State the preparation type.
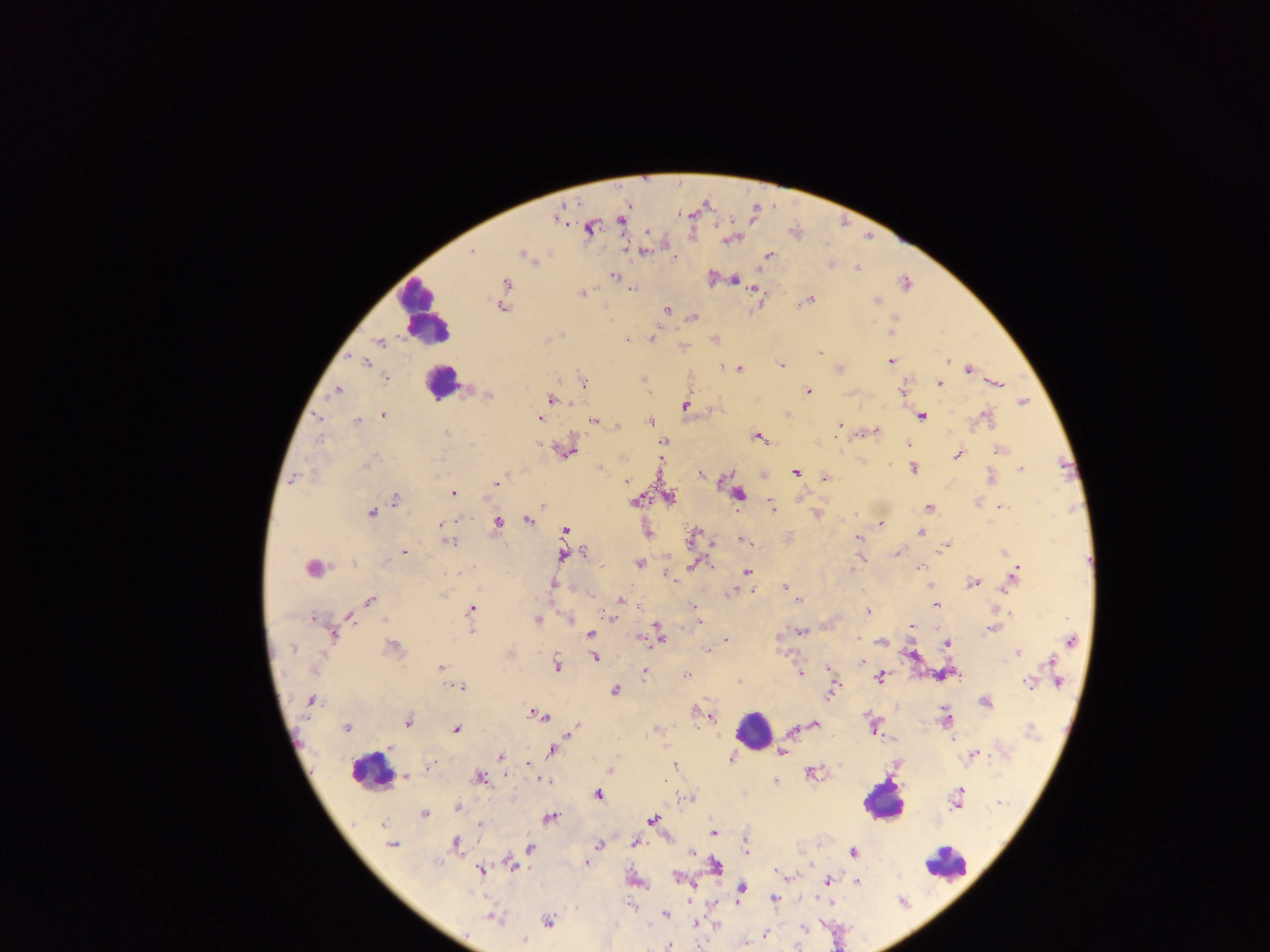

This is a thick smear.

Approximate centers as {x, y} in pixels. Leukocyte locations: {424, 313}, {441, 382}, {753, 730}, {374, 765}, {882, 801}, {948, 865}. Malaria parasite locations: {589, 228}, {646, 232}, {729, 240}, {472, 252}, {643, 252}, {522, 254}, {769, 255}, {830, 264}, {857, 267}, {614, 276}, {734, 280}, {906, 283}, {506, 284}, {633, 288}, {755, 289}, {581, 293}, {810, 300}, {876, 301}, {503, 307}, {668, 309}, {693, 317}, {893, 328}, {652, 338}, {627, 340}, {379, 342}, {820, 351}, {363, 361}, {948, 361}, {890, 362}, {781, 365}, {722, 366}, {740, 369}, {969, 369}, {839, 370}, {387, 379}, {644, 380}, {584, 382}, {998, 383}, {938, 384}, {337, 390}, {807, 391}, {901, 391}, {489, 396}, {552, 399}, {1022, 402}, {685, 405}, {788, 414}, {384, 415}, {922, 417}, {985, 417}, {317, 418}, {540, 418}, {357, 421}, {593, 421}, {650, 422}, {840, 425}, {617, 426}, {875, 431}, {446, 432}, {759, 438}, {664, 441}, {908, 444}, {472, 446}, {568, 451}, {1000, 451}, {957, 455}, {913, 468}, {599, 469}, {1021, 469}, {796, 472}, {701, 475}, {292, 478}, {824, 478}, {990, 479}, {723, 480}, {626, 481}, {497, 483}, {453, 493}, {739, 494}, {669, 497}, {395, 499}, {636, 501}, {542, 505}, {771, 506}, {1000, 507}, {929, 508}, {371, 513}, {815, 514}, {528, 521}, {496, 523}, {441, 524}, {881, 524}, {565, 531}, {648, 533}, {921, 533}, {694, 534}, {857, 537}, {742, 539}, {449, 542}, {947, 545}, {404, 552}, {584, 552}, {1004, 553}, {897, 554}, {562, 556}, {351, 562}, {638, 564}, {693, 564}, {311, 567}, {920, 567}, {852, 570}, {747, 571}, {1015, 575}, {669, 578}, {972, 582}, {552, 584}, {786, 587}, {731, 591}, {750, 591}, {441, 595}, {620, 600}, {370, 601}, {797, 601}, {937, 605}, {695, 607}, {472, 609}, {868, 611}, {350, 616}, {312, 618}, {611, 618}, {383, 619}, {537, 620}, {699, 621}, {911, 625}, {991, 629}, {472, 631}, {659, 632}, {802, 632}, {590, 634}, {334, 636}, {660, 638}, {727, 639}, {647, 640}, {1070, 640}, {880, 642}, {947, 644}, {394, 647}, {293, 648}, {707, 650}, {1018, 651}, {511, 654}, {594, 657}, {862, 660}, {1053, 662}, {556, 665}, {441, 667}, {315, 668}, {828, 668}, {644, 672}, {800, 673}, {1056, 673}, {686, 675}, {881, 677}, {1059, 681}, {739, 682}, {1027, 683}, {461, 686}, {616, 690}, {832, 692}, {312, 701}, {985, 702}, {540, 715}, {710, 717}, {945, 718}, {407, 721}, {815, 724}, {346, 728}, {574, 728}, {457, 729}, {655, 729}, {794, 731}, {570, 732}, {1031, 732}, {953, 740}, {552, 751}, {782, 752}, {973, 755}, {500, 756}, {731, 759}, {429, 766}, {674, 766}, {610, 769}, {812, 773}, {405, 777}, {481, 778}, {543, 781}, {775, 781}, {598, 795}, {957, 797}, {689, 799}, {999, 803}, {457, 808}, {425, 813}, {551, 818}, {652, 819}, {479, 825}, {714, 832}, {455, 843}, {600, 843}, {635, 843}, {392, 845}, {746, 846}, {530, 847}, {853, 852}, {692, 854}, {586, 863}, {512, 865}, {715, 866}, {481, 871}, {677, 877}, {828, 881}, {857, 882}, {742, 889}, {774, 899}, {630, 905}, {666, 914}, {492, 918}, {549, 920}, {803, 928}, {766, 935}, {524, 941}, {669, 946}. Photographed through a microscope with a mobile-phone camera. Image is 1270×952 pixels. Collected in Ghana. One field of view.